Outline every leukocyte.
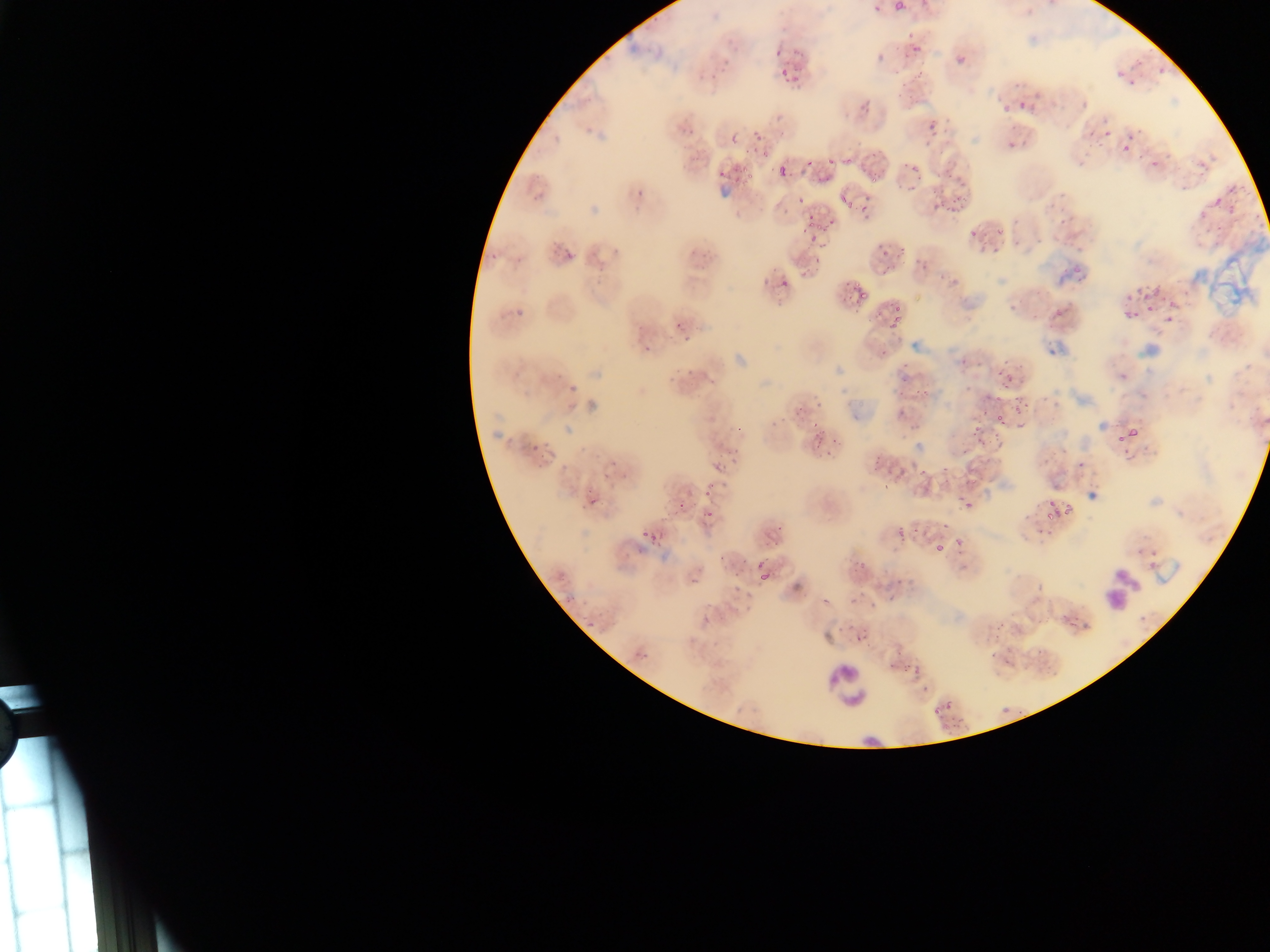
Approximate bounding boxes as left top right bottom in pixels.
Leukocytes: 1093 564 1146 615; 824 659 871 713.

Summary:
  - Plasmodium parasite locations: 896 0 908 12; 874 3 883 10; 905 31 918 42; 905 44 929 52; 791 47 808 55; 956 56 965 65; 1113 63 1122 79; 777 66 791 77; 901 68 928 89; 1158 68 1166 77; 784 76 801 87; 1124 77 1136 84; 1017 99 1029 108; 859 100 874 112; 1077 101 1089 113; 1000 103 1008 112; 927 123 935 134; 1105 130 1114 140; 1082 132 1095 135; 1124 132 1133 144; 731 135 739 144; 1095 138 1109 152; 1120 143 1130 152; 1009 146 1016 155; 761 149 771 160; 840 149 854 166; 1163 150 1171 161; 806 151 817 167; 826 158 836 166; 775 160 790 179; 1149 161 1160 173; 906 162 920 174; 737 167 750 176; 747 173 755 186; 865 173 877 183; 813 175 831 183; 905 183 922 194; 1225 186 1237 199; 848 191 856 213; 837 194 846 206; 937 196 969 216; 1208 198 1221 212; 1047 199 1055 209; 1224 206 1234 220; 1196 210 1207 221; 805 217 818 228; 1010 219 1021 227; 1056 219 1067 228; 821 220 834 237; 981 229 987 243; 993 229 1007 240; 1203 229 1211 235; 969 230 975 239; 1011 233 1022 250; 808 235 819 246; 550 236 578 262; 1066 238 1075 254; 899 243 902 262; 991 244 998 258; 878 245 893 254; 487 252 497 260; 1071 265 1080 275; 882 266 896 280; 1073 272 1087 285; 777 273 788 290; 1138 281 1153 289; 851 284 868 307; 1124 291 1135 301; 1145 296 1159 312; 1166 297 1178 306; 893 301 901 323; 513 302 525 319; 1122 307 1140 321; 1050 312 1069 323; 671 317 682 331; 886 322 896 336; 680 332 692 343; 642 333 654 357; 682 367 691 377; 997 368 1002 377; 710 375 717 387; 1000 378 1013 391; 566 379 580 393; 914 380 933 402; 1013 402 1029 411; 979 407 992 415; 997 408 1013 424; 1016 420 1026 431; 973 422 983 436; 1130 424 1143 443; 735 426 741 434; 530 428 550 454; 992 428 1001 441; 1114 431 1125 443; 814 433 826 443; 976 439 984 443; 825 452 833 460; 706 462 726 483; 917 467 926 481; 964 474 978 484; 704 488 712 496; 587 495 600 508; 954 496 967 505; 679 500 687 510; 1045 500 1055 507; 966 503 974 515; 1065 503 1075 514; 1045 507 1059 524; 704 508 712 516; 773 516 791 534; 941 522 949 534; 639 524 652 542; 890 529 910 546; 651 538 660 547; 953 538 964 545; 936 544 943 552; 756 559 766 567; 851 563 861 577; 551 568 568 583; 759 570 769 585; 887 575 908 589; 566 591 580 607; 868 601 876 609; 580 624 591 637; 850 632 868 650; 636 644 653 661; 989 645 998 660; 1034 651 1046 659; 884 655 899 672; 901 661 912 671; 912 665 922 679; 920 686 932 697; 943 696 954 715; 1000 704 1013 717; 928 707 939 718 | approximate x y pixel centers of objects too small to bound: 1139 61; 1089 145; 1080 166; 979 252; 1165 323; 997 399; 1006 663
  - Preparation: thin blood film
  - Capture: mobile-phone photograph through a microscope
  - Field of view: single
  - Country: Ghana
  - Image size: 1270×952 pixels